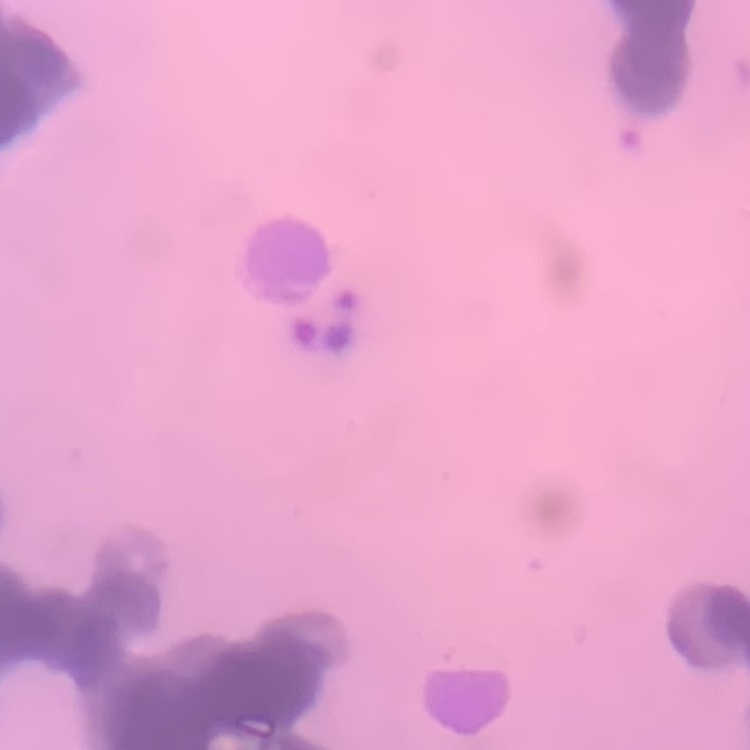
erythrocyte morphology = rouleaux formation
image type = square crop of a larger photomicrograph
stain = Field's or Giemsa
preparation = thin blood smear